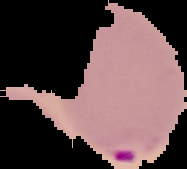
image type = cell region segmented out of the field of view; surrounding area masked to black
preparation = thin blood film
result = Plasmodium parasites identified
image size = 187×169 pixels